Identify the parasite.
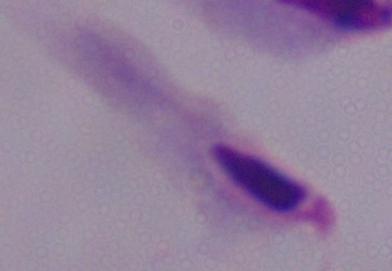
A trichomonad.

Summary:
  - Magnification: 1000x
  - Modality: photomicrograph